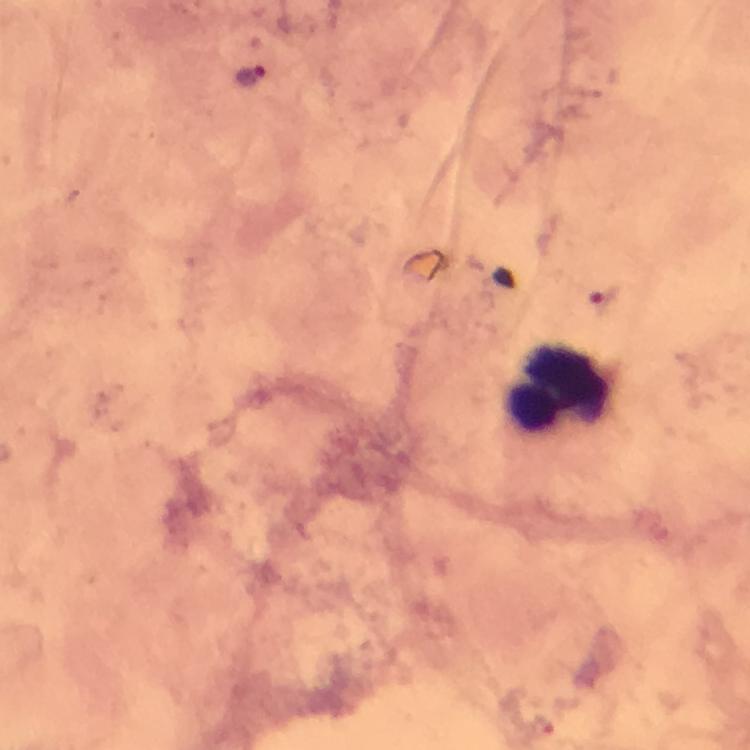
image size = 750×750 pixels
leukocyte locations = approximate object centers, in pixels from the top-left corner: (x=558, y=388)
stain = Giemsa
preparation = thick blood film
magnification = 100x
malaria parasite locations = approximate object centers, in pixels from the top-left corner: (x=249, y=75), (x=605, y=297), (x=542, y=722)
cropped from = a single field of view
capture = smartphone mounted on the microscope
context = from a malaria diagnostic workup
immersion oil = used